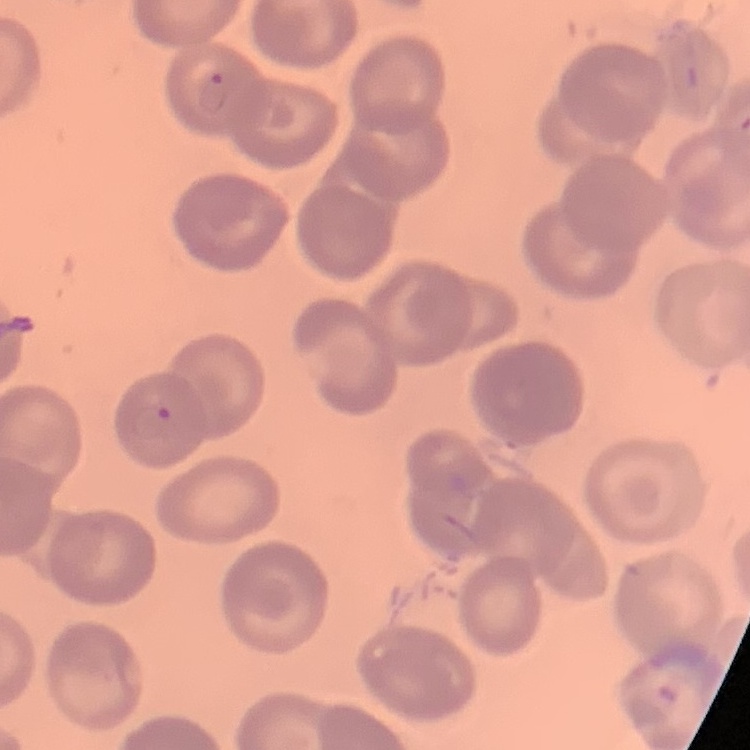

The erythrocytes exhibit no rouleaux formation. Thin blood smear. Field's or Giemsa stain. One tile cut from a larger photomicrograph.